Report the malaria status of this cell.
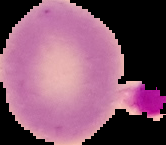

Uninfected.

Image is 166×145 pixels. From a thin blood smear. The area outside the segmented cell region is set to black.